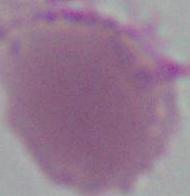
identification = red blood cell
modality = micrograph
magnification = 1000x